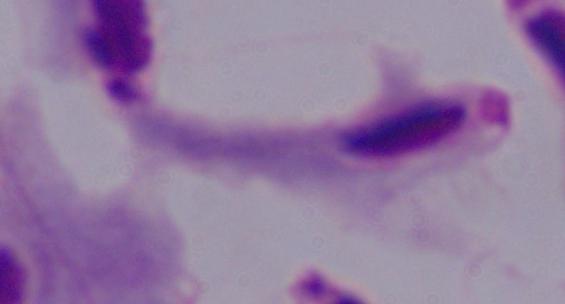 1000x magnification. A trichomonad is seen. Photomicrograph.